Identify the cell.
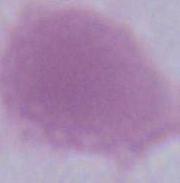
An erythrocyte.

Captured at 1000x magnification. Micrograph.